State which parasite is depicted.
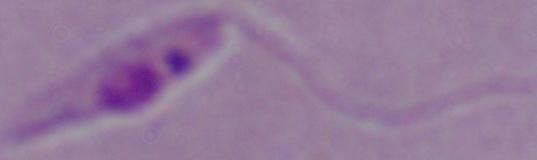

This is Leishmania.

Photomicrograph. 1000x magnification.